Assess the morphology of the red blood cells.
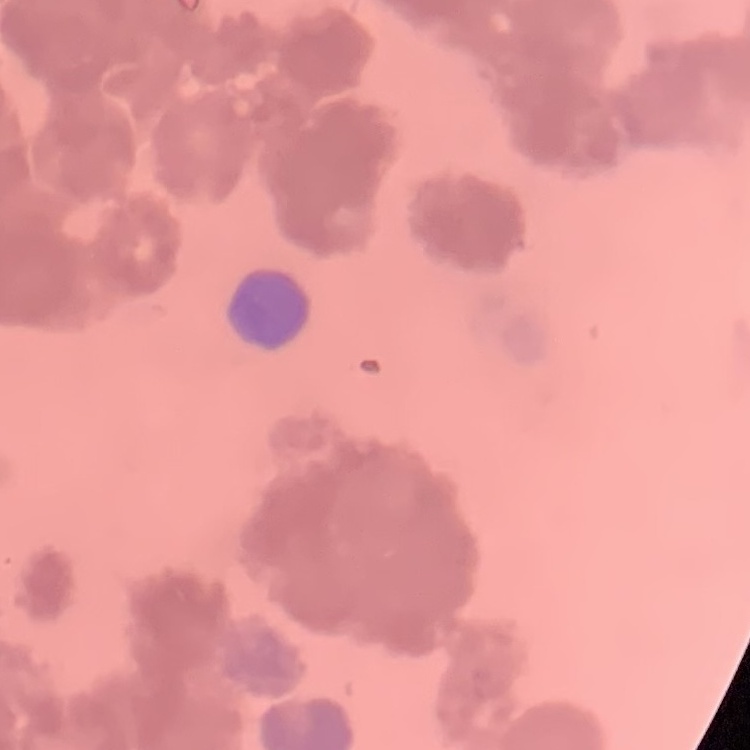
Rouleaux formation.

Summary:
  - Stain: Field's or Giemsa
  - Preparation: thin blood smear
  - Image type: one tile cut from a larger photomicrograph